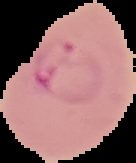

image size = 136×163 pixels
preparation = thin blood smear
image type = segmented cell region on a black background
result = malaria parasites detected